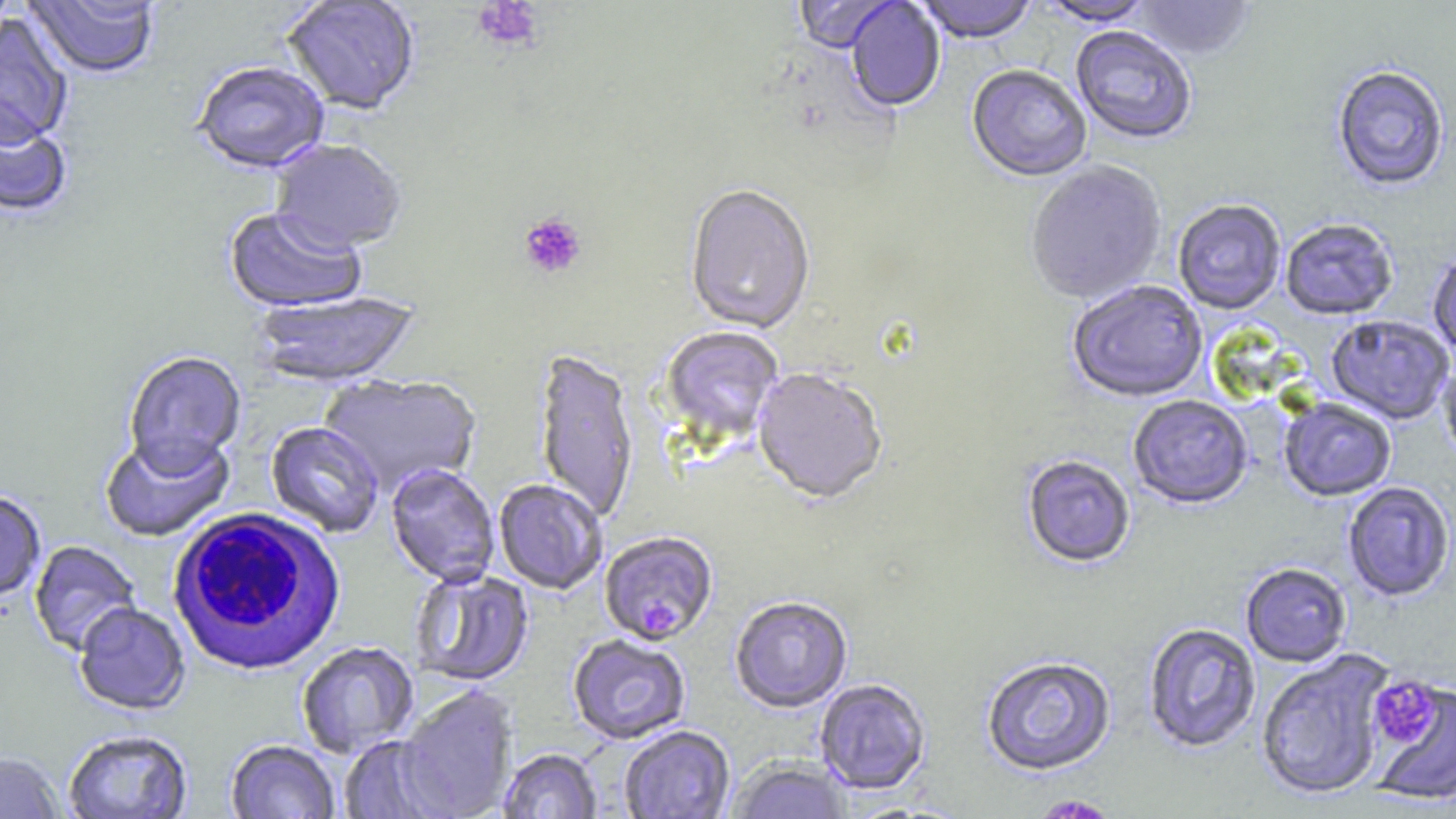
Approximate bounding boxes as (x1, y1, x2, y2) in pixels. White blood cell locations: (167, 507, 349, 678). Plasmodium falciparum-infected red blood cell locations: (599, 533, 718, 647). Platelet locations: (473, 0, 543, 52), (518, 212, 587, 279), (1370, 676, 1441, 748), (1031, 795, 1119, 818). Uninfected red blood cell locations: (25, 0, 160, 81), (281, 0, 420, 117), (793, 0, 902, 55), (915, 0, 1039, 46), (1036, 0, 1156, 28), (1133, 0, 1255, 62), (845, 1, 946, 114), (0, 16, 73, 152), (1070, 27, 1196, 146), (192, 64, 330, 176), (966, 66, 1091, 184), (1332, 67, 1450, 193), (0, 116, 73, 220), (269, 140, 407, 257), (1026, 163, 1167, 306), (684, 186, 816, 336), (1173, 201, 1286, 316), (223, 209, 366, 315), (1281, 221, 1398, 322), (1428, 249, 1456, 359), (1067, 282, 1208, 404), (252, 292, 422, 390), (1326, 316, 1454, 426), (658, 327, 784, 448), (533, 351, 640, 526), (123, 352, 246, 477), (1438, 354, 1456, 466), (752, 370, 888, 507), (319, 374, 482, 499), (1128, 396, 1252, 511), (1279, 400, 1396, 503), (265, 422, 384, 538), (99, 433, 235, 544), (1023, 457, 1135, 570), (386, 465, 499, 587), (493, 479, 607, 595), (1343, 484, 1455, 603), (0, 492, 46, 603), (29, 541, 142, 657), (1241, 564, 1351, 668), (410, 569, 534, 688), (730, 598, 853, 714), (74, 604, 190, 716), (1143, 624, 1261, 753), (568, 635, 690, 745), (297, 643, 419, 759), (1256, 650, 1393, 803), (981, 656, 1117, 778), (815, 680, 931, 796), (1369, 680, 1456, 808), (396, 686, 519, 819), (619, 726, 735, 819), (63, 731, 193, 818), (338, 735, 454, 818), (225, 740, 340, 819), (498, 749, 602, 819), (0, 752, 66, 819), (726, 759, 853, 819). Slide-level diagnosis: Plasmodium falciparum. One field of a larger specimen. Image is 1456×819 pixels. Optical microscopy. May-Grünwald-Giemsa-stained preparation. Thin blood film. Captured at 1000x magnification.